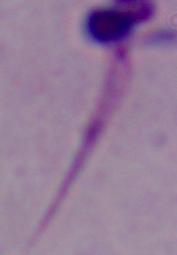
Micrograph. A Leishmania parasite is seen. 1000x magnification.